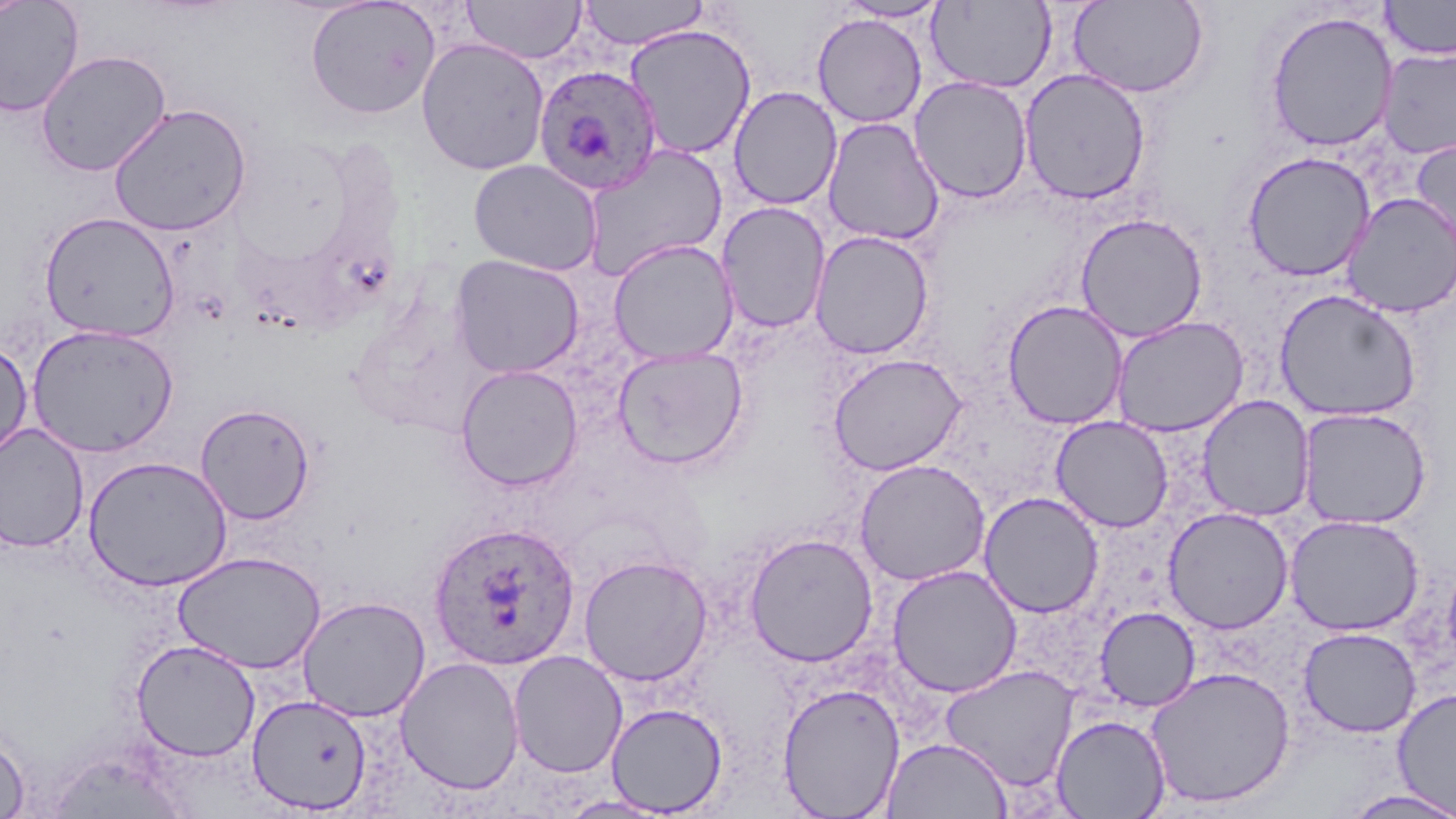

Summary:
  - Coordinate format: approximate bounding boxes as named x1/y1/x2/y2 corners in pixels
  - Uninfected red blood cell locations: (x1=0, y1=0, x2=84, y2=117), (x1=1, y1=0, x2=30, y2=22), (x1=305, y1=0, x2=440, y2=119), (x1=462, y1=0, x2=587, y2=65), (x1=1068, y1=0, x2=1209, y2=98), (x1=1380, y1=0, x2=1456, y2=60), (x1=579, y1=1, x2=709, y2=50), (x1=834, y1=1, x2=951, y2=22), (x1=927, y1=1, x2=1056, y2=92), (x1=444, y1=4, x2=579, y2=116), (x1=1263, y1=10, x2=1399, y2=152), (x1=812, y1=13, x2=927, y2=128), (x1=624, y1=24, x2=757, y2=160), (x1=416, y1=37, x2=550, y2=175), (x1=1377, y1=46, x2=1456, y2=159), (x1=36, y1=49, x2=172, y2=177), (x1=1019, y1=68, x2=1151, y2=205), (x1=909, y1=76, x2=1033, y2=203), (x1=728, y1=86, x2=843, y2=210), (x1=109, y1=104, x2=251, y2=236), (x1=822, y1=117, x2=944, y2=246), (x1=1410, y1=136, x2=1456, y2=263), (x1=582, y1=145, x2=728, y2=280), (x1=1241, y1=150, x2=1376, y2=281), (x1=467, y1=159, x2=602, y2=275), (x1=1340, y1=193, x2=1456, y2=318), (x1=716, y1=202, x2=831, y2=333), (x1=39, y1=212, x2=180, y2=342), (x1=1075, y1=213, x2=1208, y2=343), (x1=809, y1=230, x2=935, y2=360), (x1=609, y1=240, x2=738, y2=364), (x1=450, y1=254, x2=585, y2=378), (x1=1274, y1=289, x2=1422, y2=422), (x1=1002, y1=299, x2=1129, y2=430), (x1=1110, y1=316, x2=1249, y2=436), (x1=27, y1=324, x2=179, y2=457), (x1=0, y1=338, x2=33, y2=461), (x1=612, y1=345, x2=748, y2=470), (x1=827, y1=353, x2=967, y2=476), (x1=456, y1=364, x2=583, y2=491), (x1=1197, y1=395, x2=1315, y2=522), (x1=195, y1=403, x2=316, y2=525), (x1=1297, y1=406, x2=1432, y2=529), (x1=1050, y1=416, x2=1174, y2=532), (x1=0, y1=423, x2=90, y2=553), (x1=83, y1=456, x2=233, y2=592), (x1=854, y1=459, x2=991, y2=586), (x1=978, y1=491, x2=1104, y2=618), (x1=1163, y1=506, x2=1294, y2=633), (x1=1285, y1=514, x2=1425, y2=636), (x1=743, y1=532, x2=878, y2=667), (x1=173, y1=551, x2=326, y2=674), (x1=578, y1=554, x2=713, y2=686), (x1=1442, y1=554, x2=1456, y2=674), (x1=887, y1=564, x2=1023, y2=698), (x1=297, y1=595, x2=431, y2=721), (x1=1095, y1=606, x2=1200, y2=711), (x1=1298, y1=627, x2=1421, y2=738), (x1=130, y1=639, x2=259, y2=761), (x1=508, y1=649, x2=628, y2=778), (x1=395, y1=656, x2=524, y2=795), (x1=939, y1=665, x2=1079, y2=791), (x1=1145, y1=666, x2=1295, y2=808), (x1=777, y1=683, x2=906, y2=818), (x1=1392, y1=688, x2=1456, y2=816), (x1=247, y1=693, x2=373, y2=814), (x1=605, y1=702, x2=728, y2=816), (x1=1051, y1=714, x2=1171, y2=819), (x1=0, y1=726, x2=30, y2=819), (x1=882, y1=736, x2=1012, y2=818), (x1=1339, y1=789, x2=1456, y2=819), (x1=555, y1=794, x2=675, y2=818)
  - Plasmodium ovale-infected red blood cell locations: (x1=532, y1=63, x2=663, y2=196), (x1=428, y1=521, x2=581, y2=670)
  - Slide-level diagnosis: Plasmodium ovale
  - Preparation: thin blood film
  - Field of view: single
  - Modality: light microscopy
  - Image size: 1456×819 pixels
  - Magnification: 1000x
  - Stain: May-Grünwald-Giemsa